Locate every blood parasite and identify its species.
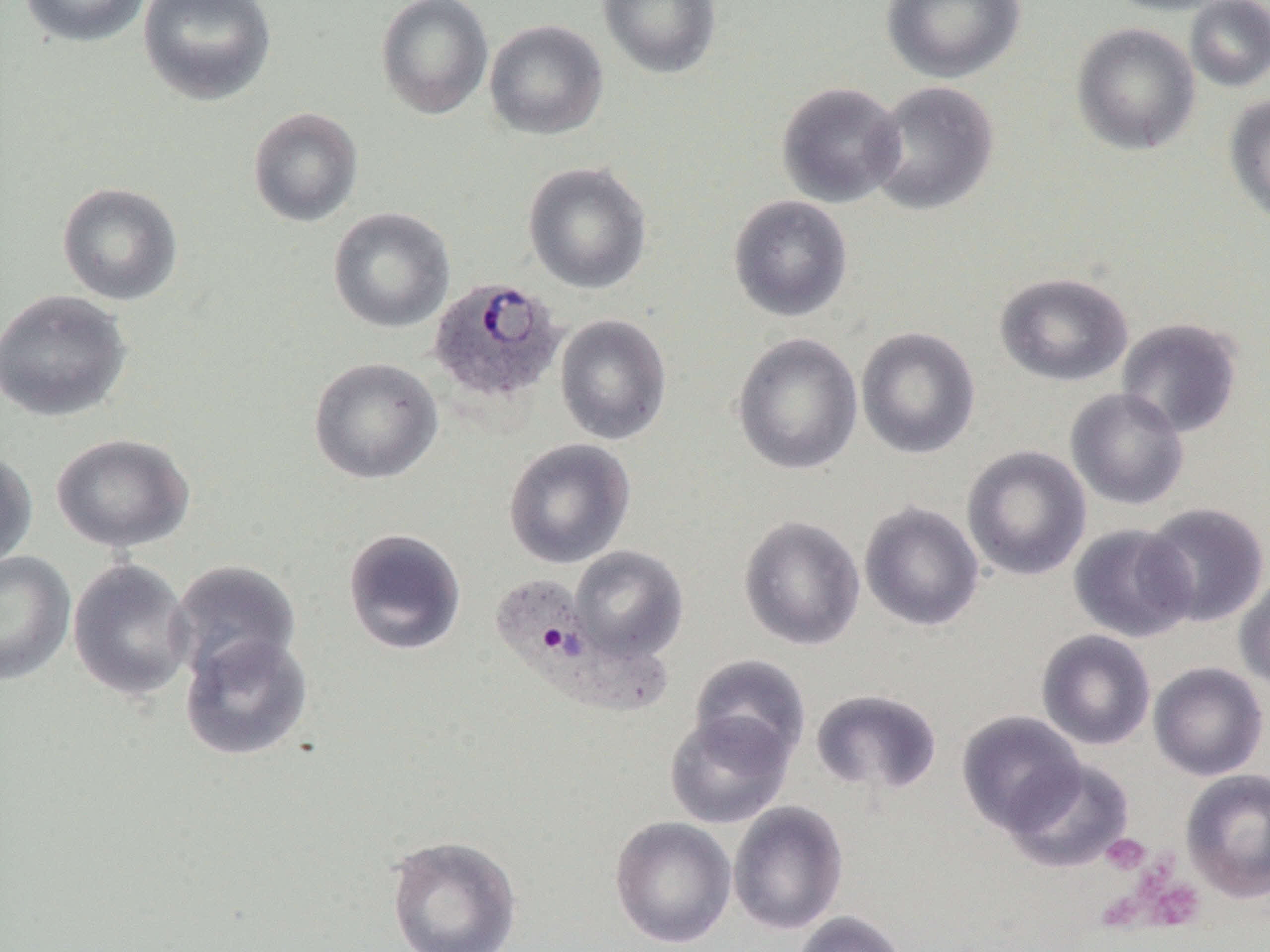

Approximate bounding boxes as (x1, y1, x2, y2) in pixels.
Plasmodium ovale-infected red blood cells: (428, 277, 565, 405), (494, 579, 670, 719).
No Plasmodium falciparum, Plasmodium malariae, Plasmodium vivax, Babesia divergens, or Trypanosoma brucei observed.

{
  "slide_level_diagnosis": "Plasmodium ovale",
  "magnification": "1000x",
  "preparation": "thin blood film",
  "platelet_locations": "approximate bounding boxes as (x1, y1, x2, y2) in pixels: (1102, 834, 1150, 874), (1144, 875, 1206, 928)",
  "field_of_view": "single",
  "uninfected_red_blood_cell_locations": "approximate bounding boxes as (x1, y1, x2, y2) in pixels: (19, 0, 153, 48), (138, 0, 277, 106), (375, 0, 494, 119), (598, 0, 722, 80), (882, 0, 1026, 84), (1102, 0, 1235, 16), (1185, 0, 1270, 92), (484, 19, 608, 140), (1071, 22, 1200, 155), (867, 79, 999, 216), (776, 81, 906, 208), (1223, 95, 1270, 227), (247, 107, 364, 227), (523, 161, 652, 294), (57, 182, 184, 305), (728, 195, 853, 321), (328, 207, 455, 333), (994, 272, 1134, 387), (0, 289, 133, 422), (555, 314, 672, 445), (1116, 317, 1243, 438), (855, 327, 981, 459), (732, 332, 864, 475), (309, 358, 442, 484), (1066, 387, 1189, 510), (51, 433, 195, 553), (503, 438, 635, 569), (962, 445, 1092, 581), (0, 448, 37, 570), (859, 501, 984, 632), (1140, 502, 1269, 627), (738, 515, 866, 651), (1068, 524, 1196, 643), (342, 528, 467, 655), (570, 546, 689, 662), (0, 551, 76, 685), (67, 558, 195, 701), (167, 560, 301, 686), (1234, 572, 1270, 693), (1036, 629, 1156, 751), (179, 632, 314, 761), (690, 654, 811, 764), (1148, 661, 1269, 781), (811, 689, 943, 797), (665, 710, 794, 829), (957, 710, 1086, 835), (1004, 758, 1135, 872), (1180, 768, 1270, 904), (727, 800, 849, 935), (609, 816, 737, 949), (385, 834, 523, 952), (791, 910, 910, 952)",
  "modality": "light microscopy",
  "image_size": "1270×952 pixels"
}